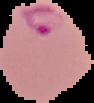

preparation = thin blood smear
image size = 94×103 pixels
image type = cell region segmented out of the field of view; surrounding area masked to black
malaria status = parasitized